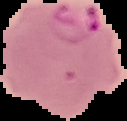
Summary:
  - Image type: segmented cell region with the area outside set to black
  - Image size: 127×121 pixels
  - Malaria status: parasitized
  - Preparation: thin blood smear